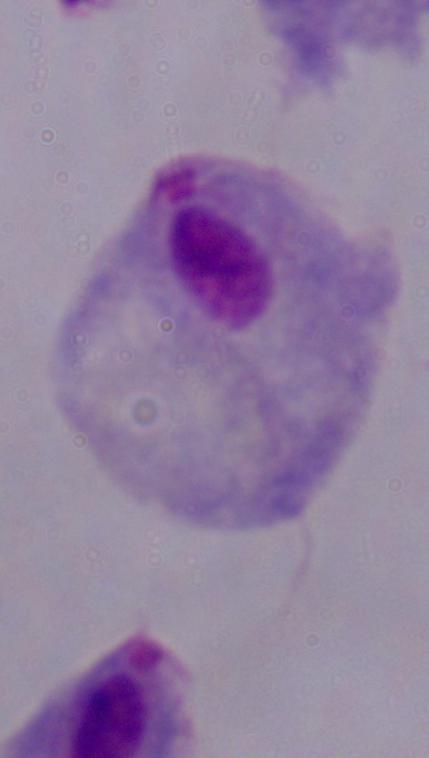
{
  "identification": "trichomonad",
  "modality": "photomicrograph",
  "magnification": "1000x"
}